Give the extent of all Plasmodium falciparum-infected red blood cells.
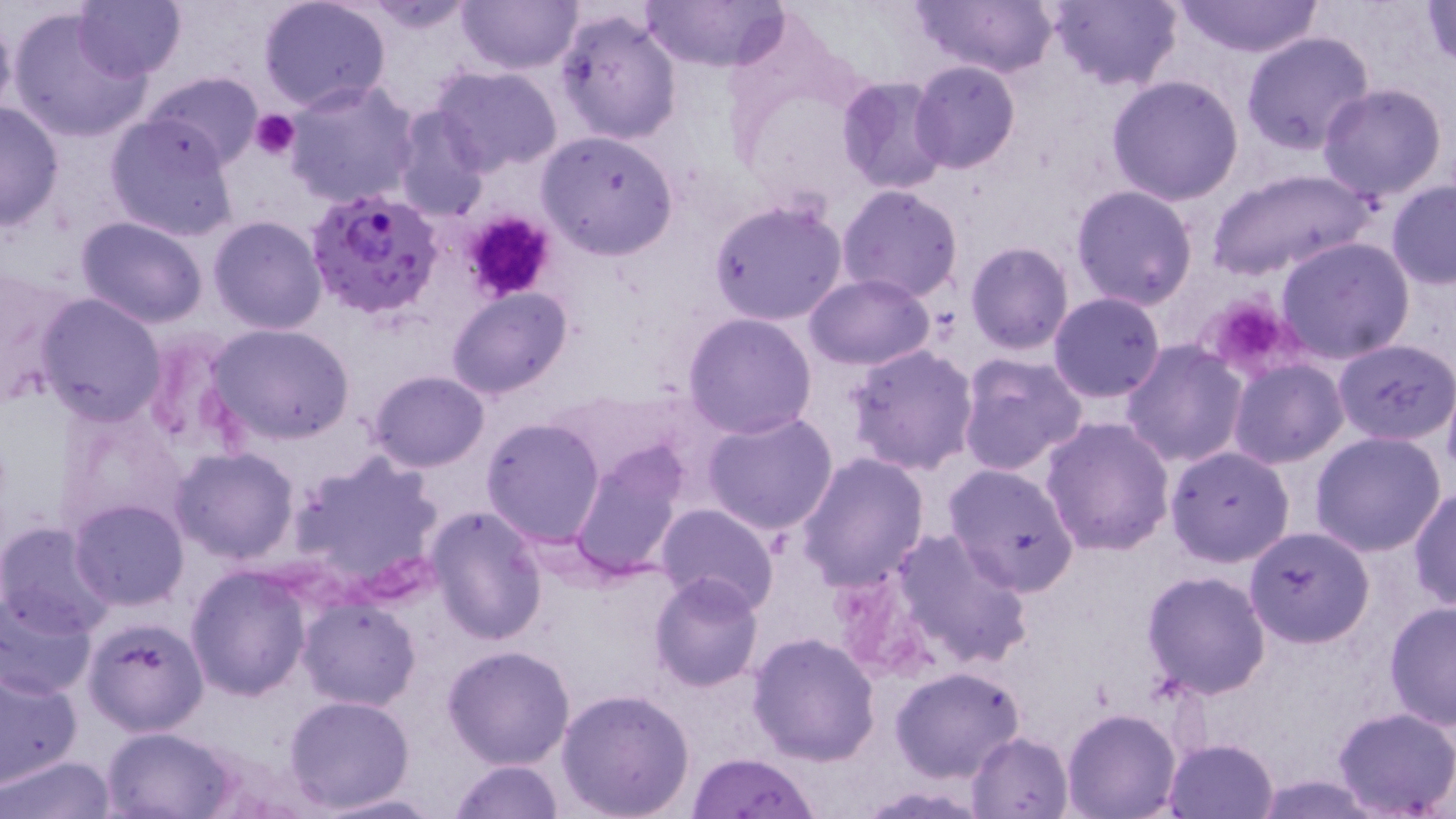
Approximate bounding boxes as (x1,y1)-(x2,y2) corner pairs in pixels.
Plasmodium falciparum-infected red blood cells: (306,187)-(443,320).

Uninfected red blood cell locations: (72,0)-(186,81), (258,0)-(392,114), (456,0)-(583,76), (640,0)-(787,73), (910,0)-(1060,77), (1043,0)-(1183,91), (1172,0)-(1323,58), (1423,1)-(1455,69), (6,6)-(155,145), (0,7)-(18,126), (554,7)-(683,144), (1241,32)-(1376,156), (909,60)-(1021,174), (432,66)-(563,176), (142,69)-(265,168), (835,75)-(951,195), (1106,76)-(1245,207), (283,79)-(420,208), (1317,83)-(1448,202), (1,98)-(63,234), (391,105)-(490,222), (104,115)-(237,242), (536,129)-(680,260), (1206,168)-(1377,281), (1386,181)-(1456,288), (837,184)-(965,302), (1070,185)-(1198,311), (707,199)-(849,326), (208,215)-(328,336), (76,216)-(209,328), (1277,235)-(1415,364), (965,241)-(1075,355), (0,271)-(80,405), (802,274)-(935,370), (446,287)-(574,400), (1048,291)-(1165,402), (35,294)-(167,425), (682,311)-(817,439), (208,324)-(354,444), (139,330)-(253,465), (1121,338)-(1248,466), (1333,340)-(1455,445), (847,345)-(979,474), (956,353)-(1088,476), (1228,359)-(1349,469), (369,370)-(489,471), (1443,379)-(1456,490), (60,400)-(189,537), (701,409)-(841,537), (482,416)-(607,548), (1041,417)-(1174,556), (1309,432)-(1447,556), (567,444)-(690,583), (1165,446)-(1295,566), (170,447)-(299,564), (288,448)-(445,596), (796,453)-(930,592), (942,462)-(1081,595), (1411,485)-(1455,613), (69,499)-(189,610), (657,504)-(780,616), (424,506)-(548,647), (1,522)-(116,640), (1245,526)-(1376,648), (890,527)-(1032,669), (186,566)-(313,700), (1141,570)-(1273,699), (648,573)-(765,691), (0,589)-(97,702), (297,596)-(420,712), (1384,599)-(1456,732), (81,615)-(210,736), (747,630)-(881,766), (442,644)-(577,770), (0,661)-(83,787), (889,665)-(1026,782), (556,688)-(697,819), (283,694)-(415,812), (1332,707)-(1455,817), (1062,708)-(1181,818), (100,724)-(239,818), (966,730)-(1074,818), (1164,737)-(1280,819), (687,752)-(816,818), (2,755)-(117,819), (447,759)-(565,819), (306,791)-(449,817). Platelet locations: (252,110)-(302,158), (457,210)-(558,304), (1200,294)-(1301,381). Slide-level diagnosis: Plasmodium falciparum. May-Grünwald-Giemsa stain. Optical microscopy. 1000x magnification. Image is 1456×819 pixels. Thin blood smear. One field of a larger specimen.